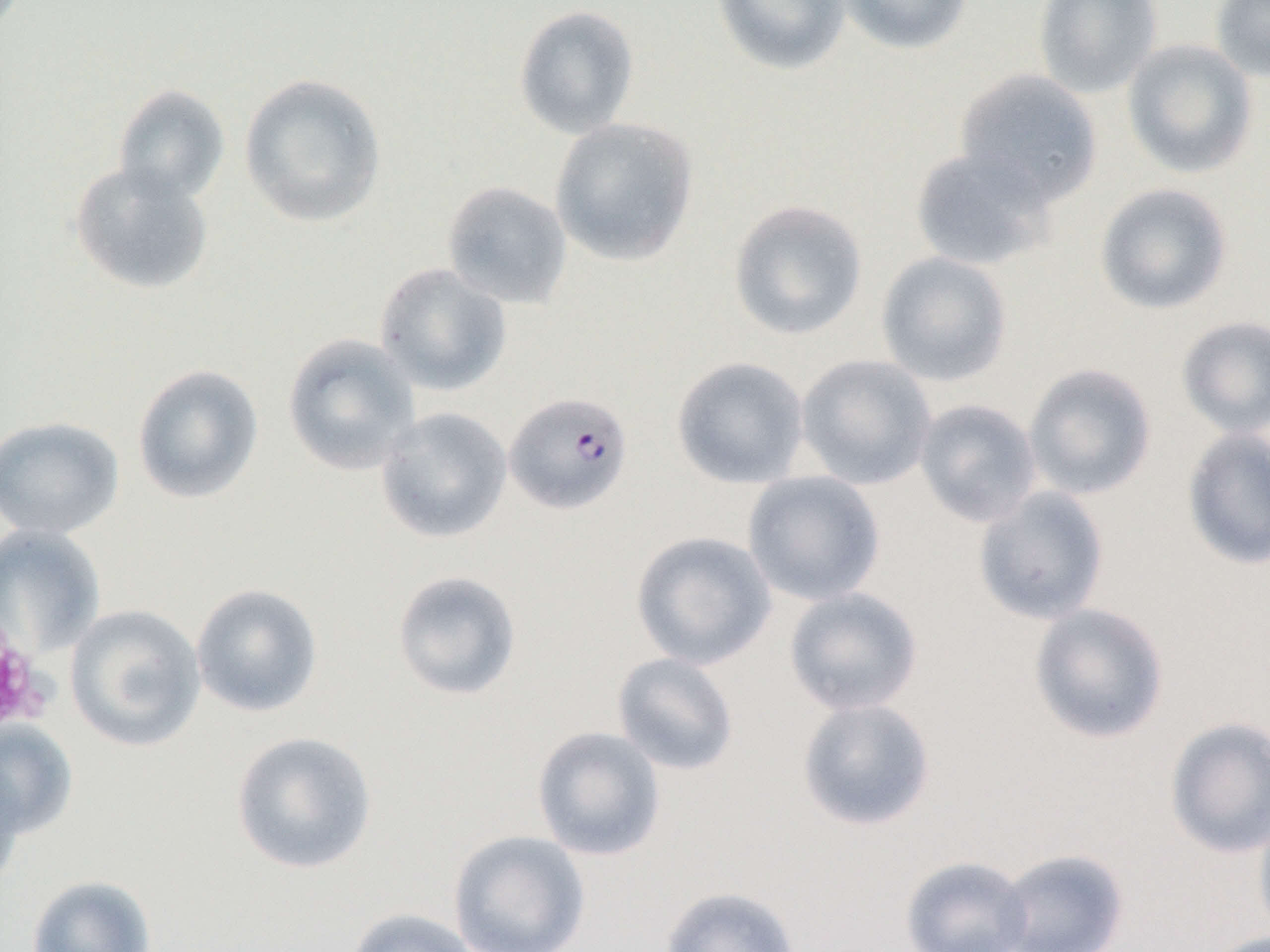
Approximate bounding boxes as (x1, y1, x2, y2) in pixels. Uninfected red blood cell locations: (711, 0, 851, 76), (836, 0, 973, 55), (1032, 0, 1162, 99), (1209, 0, 1270, 82), (513, 4, 640, 140), (1122, 39, 1258, 178), (954, 68, 1103, 207), (238, 73, 388, 228), (112, 84, 230, 205), (549, 117, 700, 267), (909, 146, 1057, 272), (69, 162, 214, 296), (441, 180, 573, 309), (1094, 183, 1233, 315), (728, 199, 868, 340), (876, 251, 1013, 387), (374, 263, 512, 396), (1176, 316, 1270, 439), (282, 333, 420, 475), (795, 354, 937, 490), (671, 356, 810, 489), (132, 363, 264, 505), (1023, 363, 1157, 501), (913, 398, 1042, 528), (376, 407, 512, 544), (0, 416, 125, 540), (1181, 427, 1270, 570), (742, 471, 886, 606), (972, 485, 1110, 625), (0, 524, 106, 659), (630, 530, 776, 670), (391, 569, 522, 701), (191, 583, 324, 717), (783, 587, 924, 716), (1028, 602, 1170, 744), (64, 604, 206, 753), (612, 652, 740, 776), (796, 697, 936, 831), (1164, 716, 1270, 859), (0, 720, 78, 839), (531, 725, 666, 861), (229, 730, 378, 875), (0, 756, 26, 891), (1253, 806, 1270, 943), (448, 829, 592, 952), (995, 848, 1129, 952), (899, 855, 1034, 952), (26, 874, 157, 952), (658, 885, 802, 952), (344, 907, 485, 952), (1204, 930, 1270, 952). Plasmodium falciparum-infected red blood cell locations: (504, 391, 634, 514). Platelet locations: (0, 617, 48, 734). Slide-level diagnosis: Plasmodium falciparum. Optical microscopy. One field of a larger specimen. Captured at 1000x magnification. Thin blood smear. Image is 1270×952 pixels.